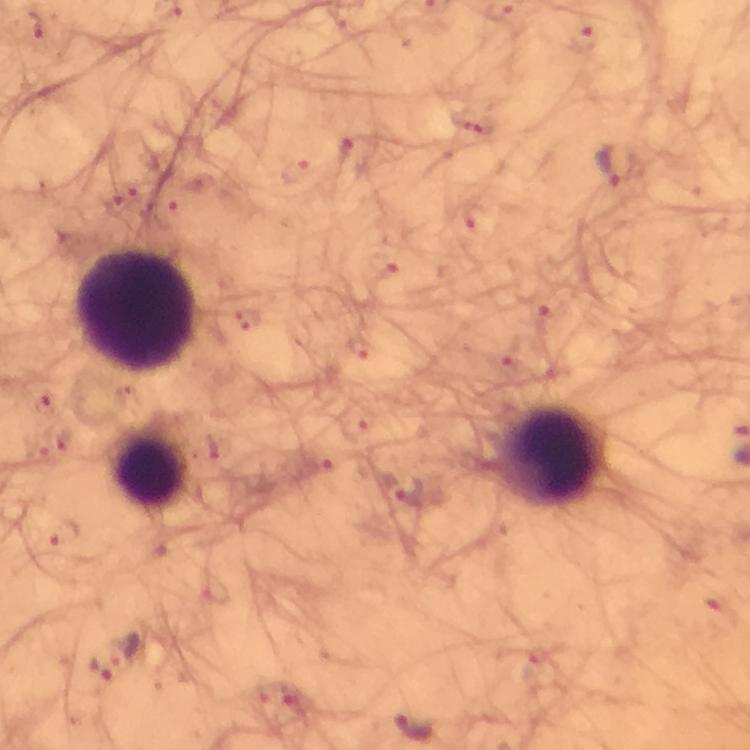

magnification = 100x
preparation = thick blood film
leukocyte locations = approximate object centers, in pixels from the top-left corner: (x=138, y=313), (x=551, y=454), (x=150, y=469)
cropped from = one field of view
immersion oil = applied
capture = smartphone photograph through a microscope
Plasmodium parasite locations = approximate object centers, in pixels from the top-left corner: (x=39, y=26), (x=615, y=167), (x=46, y=405), (x=61, y=438), (x=406, y=488), (x=65, y=536), (x=125, y=649), (x=102, y=668), (x=415, y=726)
context = from a diagnostic examination for malaria
stain = Giemsa
image size = 750×750 pixels